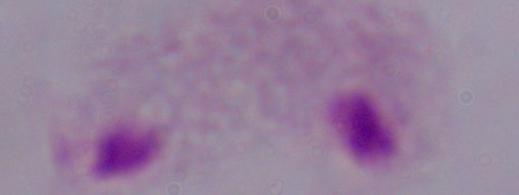
Photomicrograph. 1000x magnification. A trichomonad is shown.